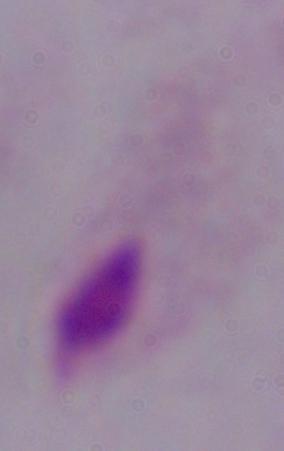

Summary:
  - Identification: trichomonad
  - Modality: photomicrograph
  - Magnification: 1000x